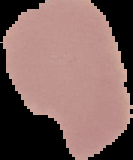

image size = 133×160 pixels
result = negative for malaria parasites
preparation = thin blood smear
image type = segmented cell region with the area outside set to black